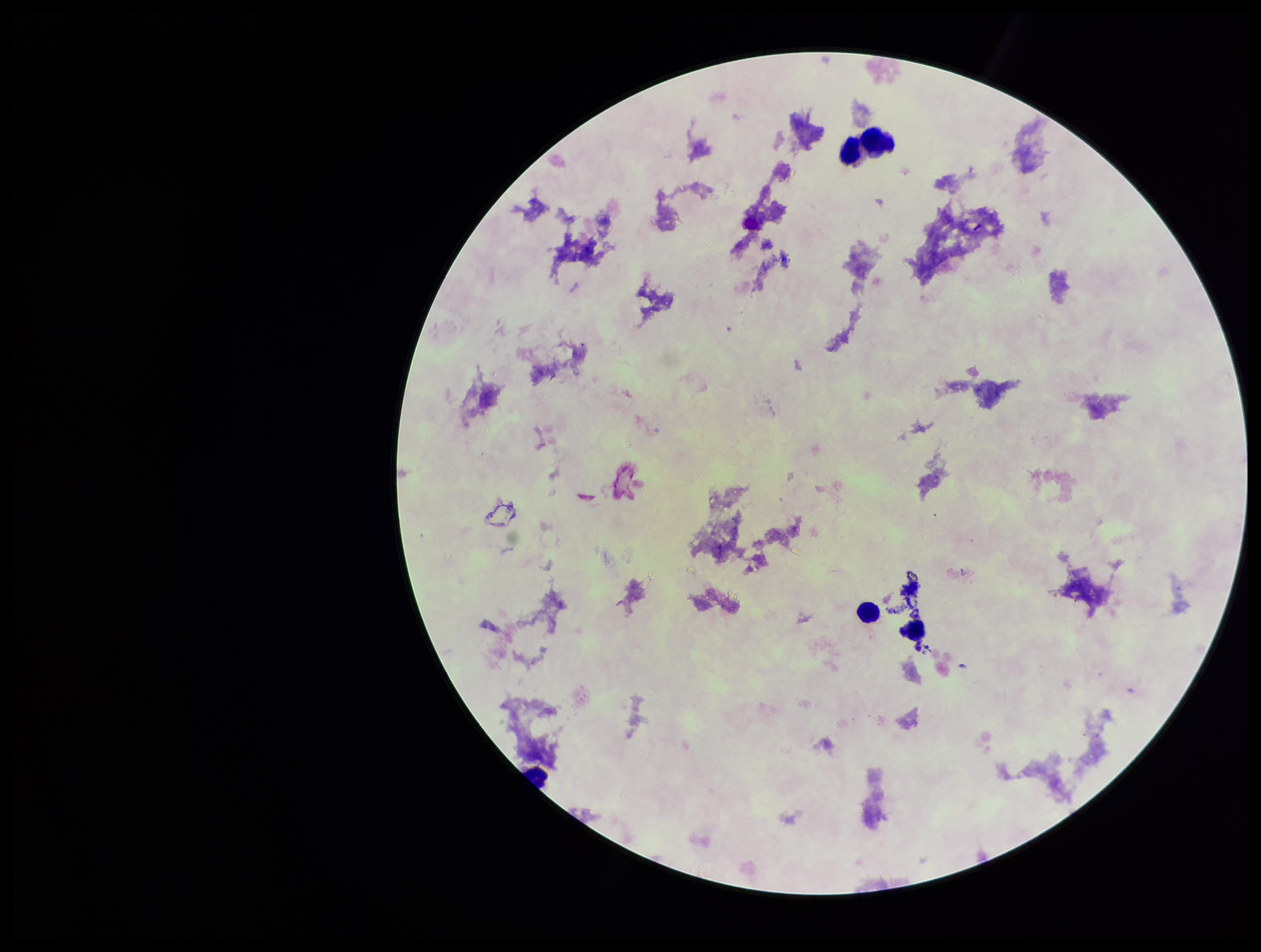
parasite count = 0
stain = Giemsa
leukocyte count = 4
Plasmodium parasites = none seen
patient malaria status = negative
field of view = single
image size = 1261×952 pixels
preparation = thick smear
capture = smartphone photograph through the microscope eyepiece